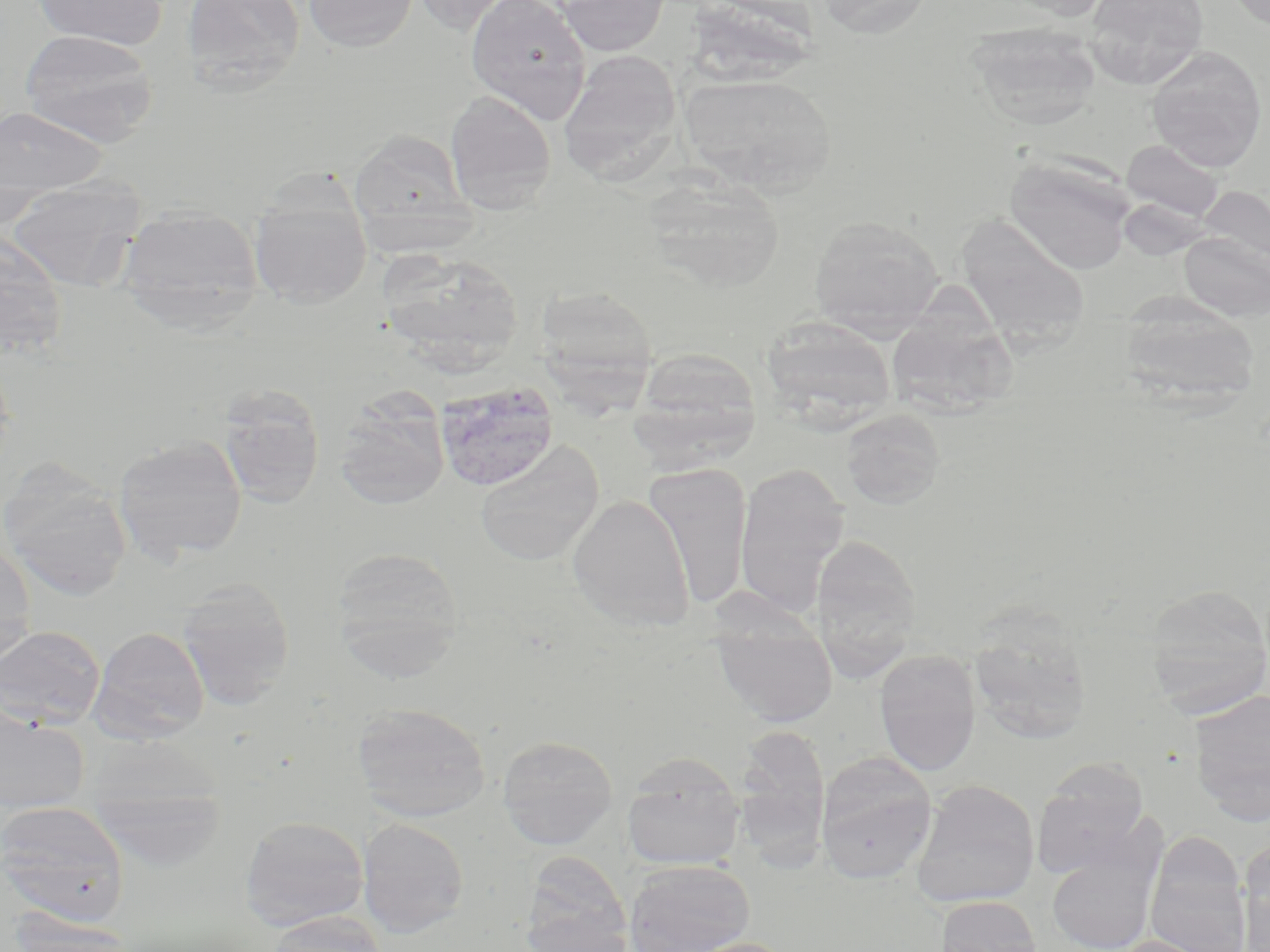
Approximate bounding boxes as named x1/y1/x2/y2 corners in pixels. Uninfected red blood cell locations: (x1=32, y1=0, x2=169, y2=50), (x1=181, y1=0, x2=306, y2=91), (x1=301, y1=0, x2=418, y2=52), (x1=407, y1=0, x2=521, y2=34), (x1=465, y1=0, x2=592, y2=123), (x1=554, y1=0, x2=671, y2=56), (x1=813, y1=0, x2=934, y2=38), (x1=997, y1=0, x2=1117, y2=20), (x1=1085, y1=0, x2=1209, y2=88), (x1=1222, y1=0, x2=1270, y2=32), (x1=690, y1=2, x2=827, y2=91), (x1=967, y1=24, x2=1101, y2=130), (x1=20, y1=29, x2=160, y2=147), (x1=1146, y1=47, x2=1267, y2=172), (x1=559, y1=50, x2=684, y2=179), (x1=678, y1=73, x2=839, y2=195), (x1=444, y1=89, x2=557, y2=214), (x1=0, y1=106, x2=109, y2=200), (x1=350, y1=130, x2=469, y2=231), (x1=1122, y1=139, x2=1225, y2=223), (x1=1003, y1=155, x2=1136, y2=275), (x1=643, y1=174, x2=786, y2=291), (x1=5, y1=176, x2=147, y2=290), (x1=1198, y1=186, x2=1270, y2=270), (x1=249, y1=193, x2=372, y2=307), (x1=116, y1=204, x2=264, y2=329), (x1=956, y1=214, x2=1091, y2=349), (x1=808, y1=215, x2=945, y2=335), (x1=1179, y1=232, x2=1270, y2=321), (x1=0, y1=233, x2=69, y2=359), (x1=376, y1=248, x2=525, y2=369), (x1=891, y1=279, x2=1027, y2=427), (x1=540, y1=287, x2=658, y2=428), (x1=1118, y1=295, x2=1261, y2=408), (x1=761, y1=317, x2=897, y2=426), (x1=631, y1=347, x2=761, y2=460), (x1=435, y1=381, x2=559, y2=491), (x1=215, y1=383, x2=326, y2=509), (x1=334, y1=392, x2=450, y2=510), (x1=840, y1=409, x2=946, y2=510), (x1=113, y1=435, x2=247, y2=565), (x1=475, y1=440, x2=604, y2=566), (x1=735, y1=461, x2=849, y2=619), (x1=643, y1=462, x2=753, y2=610), (x1=1, y1=465, x2=132, y2=602), (x1=567, y1=494, x2=695, y2=632), (x1=810, y1=534, x2=921, y2=682), (x1=0, y1=542, x2=37, y2=667), (x1=331, y1=546, x2=464, y2=676), (x1=175, y1=577, x2=295, y2=710), (x1=1142, y1=585, x2=1270, y2=716), (x1=711, y1=610, x2=838, y2=727), (x1=967, y1=611, x2=1093, y2=747), (x1=0, y1=625, x2=106, y2=730), (x1=89, y1=625, x2=209, y2=743), (x1=874, y1=649, x2=981, y2=776), (x1=1189, y1=688, x2=1270, y2=825), (x1=351, y1=702, x2=492, y2=822), (x1=0, y1=708, x2=89, y2=813), (x1=733, y1=725, x2=832, y2=865), (x1=497, y1=735, x2=618, y2=850), (x1=816, y1=752, x2=937, y2=884), (x1=621, y1=753, x2=745, y2=871), (x1=1033, y1=762, x2=1149, y2=879), (x1=87, y1=764, x2=228, y2=871), (x1=911, y1=779, x2=1040, y2=908), (x1=1, y1=801, x2=129, y2=923), (x1=240, y1=815, x2=369, y2=929), (x1=357, y1=818, x2=469, y2=937), (x1=1145, y1=833, x2=1251, y2=952), (x1=1046, y1=839, x2=1163, y2=952), (x1=1239, y1=840, x2=1270, y2=951), (x1=520, y1=851, x2=632, y2=952), (x1=623, y1=860, x2=755, y2=952), (x1=935, y1=896, x2=1043, y2=951), (x1=267, y1=911, x2=387, y2=952), (x1=12, y1=913, x2=134, y2=952), (x1=520, y1=916, x2=634, y2=952), (x1=1109, y1=935, x2=1223, y2=952), (x1=675, y1=936, x2=798, y2=952). Slide-level diagnosis: Plasmodium vivax. Image is 1270×952 pixels. Light microscopy. Captured at 1000x magnification. May-Grünwald-Giemsa-stained preparation. Thin blood smear. Single field of view.